Evaluate for malaria.
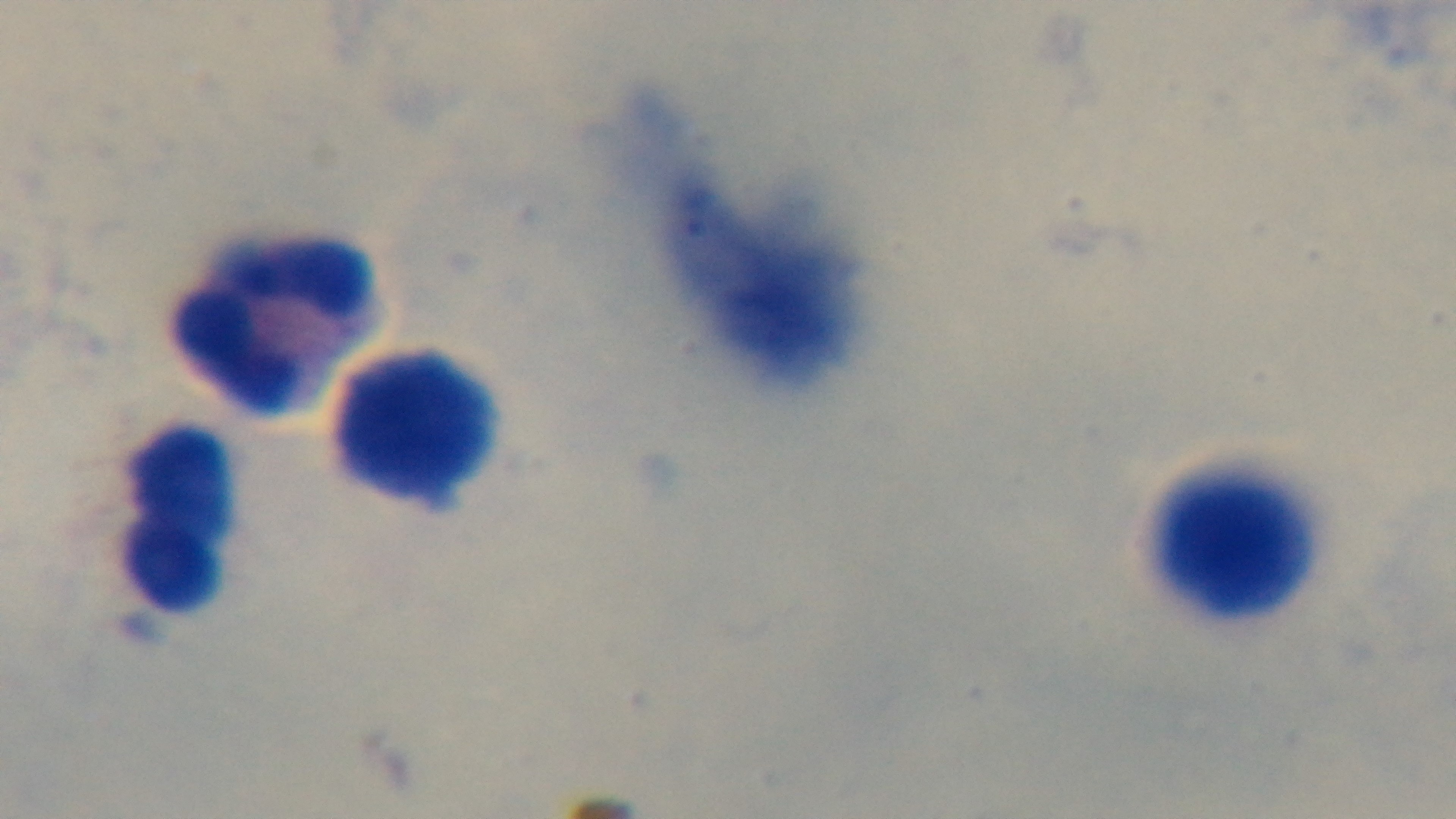
It is uninfected.

Summary:
  - Stain: Giemsa
  - Preparation: thick smear
  - Modality: light microscopy
  - Objective: 100x oil immersion
  - Capture: mounted 4K digital camera
  - Field of view: one from the slide